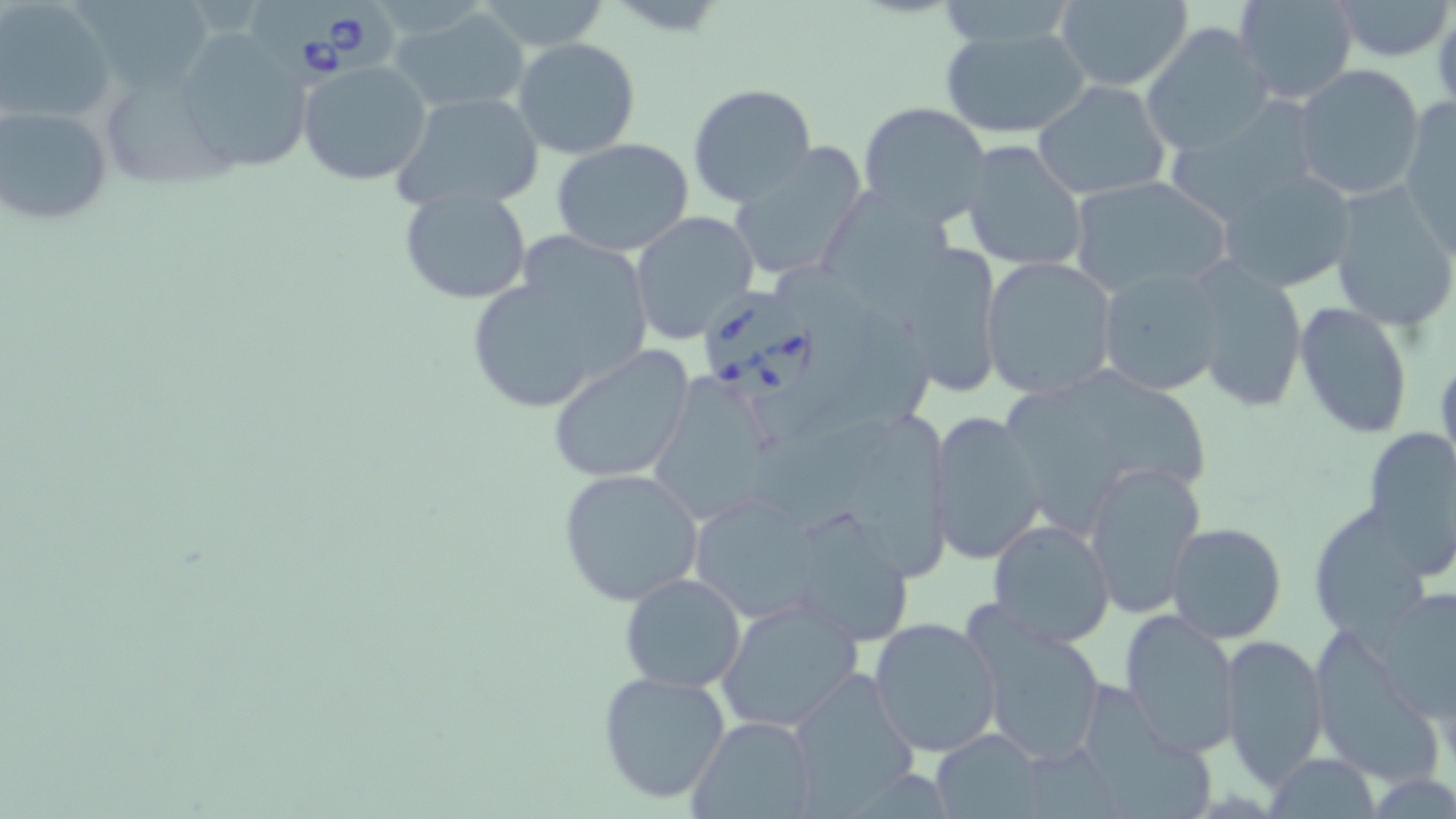

Summary:
  - Coordinate format: approximate bounding boxes as (x1,y1)-(x2,y2) corner pairs in pixels
  - Babesia divergens-infected red blood cell locations: (251,0)-(400,83), (704,289)-(821,409)
  - Uninfected red blood cell locations: (1233,0)-(1360,104), (1331,0)-(1454,63), (80,1)-(217,90), (471,1)-(611,51), (1,2)-(114,124), (1049,2)-(1194,91), (391,6)-(533,113), (1142,23)-(1273,156), (939,24)-(1091,137), (173,31)-(311,176), (512,37)-(642,158), (297,60)-(434,186), (1293,65)-(1426,200), (1033,81)-(1171,200), (687,83)-(817,207), (107,85)-(241,189), (390,91)-(545,214), (1400,98)-(1456,255), (858,100)-(991,228), (1166,100)-(1324,220), (1,106)-(114,228), (551,138)-(697,256), (960,139)-(1088,273), (728,146)-(867,283), (1215,167)-(1358,294), (1067,176)-(1232,300), (1325,180)-(1455,332), (396,184)-(534,305), (822,186)-(960,322), (630,211)-(759,343), (464,239)-(653,417), (891,242)-(1003,393), (980,255)-(1117,398), (1188,261)-(1307,413), (1095,264)-(1226,397), (1295,300)-(1414,441), (546,345)-(698,485), (1067,363)-(1211,485), (647,372)-(794,529), (1002,384)-(1122,538), (925,410)-(1046,565), (849,412)-(949,583), (1362,427)-(1456,566), (1084,460)-(1206,618), (557,467)-(704,605), (694,492)-(821,624), (1305,510)-(1434,635), (797,514)-(916,644), (987,520)-(1115,648), (1167,523)-(1287,644), (619,572)-(748,694), (1371,584)-(1456,717), (716,597)-(865,735), (1121,606)-(1241,756), (869,615)-(1003,758), (974,615)-(1108,767), (1218,632)-(1330,788), (596,669)-(732,807), (783,671)-(921,808), (1087,681)-(1219,819), (688,715)-(818,818), (930,729)-(1047,817), (1265,752)-(1378,818)
  - Slide-level diagnosis: Babesia divergens
  - Image size: 1456×819 pixels
  - Magnification: 1000x
  - Modality: optical microscopy
  - Field of view: one of a larger specimen
  - Preparation: thin blood film
  - Stain: May-Grünwald-Giemsa